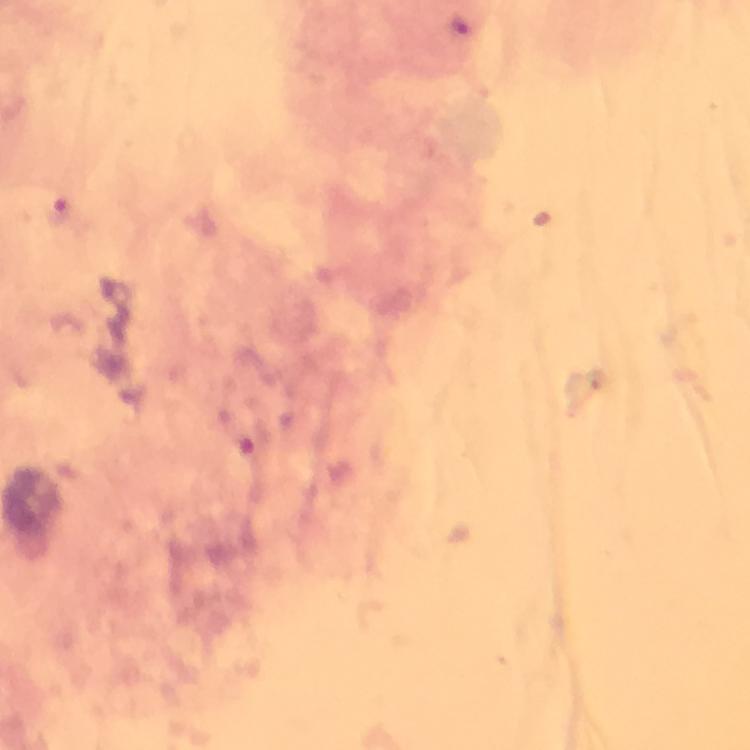
context: from a diagnostic examination for malaria
capture: smartphone mounted on the microscope
immersion_oil: used
malaria_parasite_locations: 'approximate centers as {x, y} in pixels: {459, 25}, {58, 211}'
cropped_from: a single field of view
preparation: thick smear
magnification: 100x
stain: Giemsa
image_size: 750×750 pixels